Give the extent of all Plasmodium falciparum-infected red blood cells.
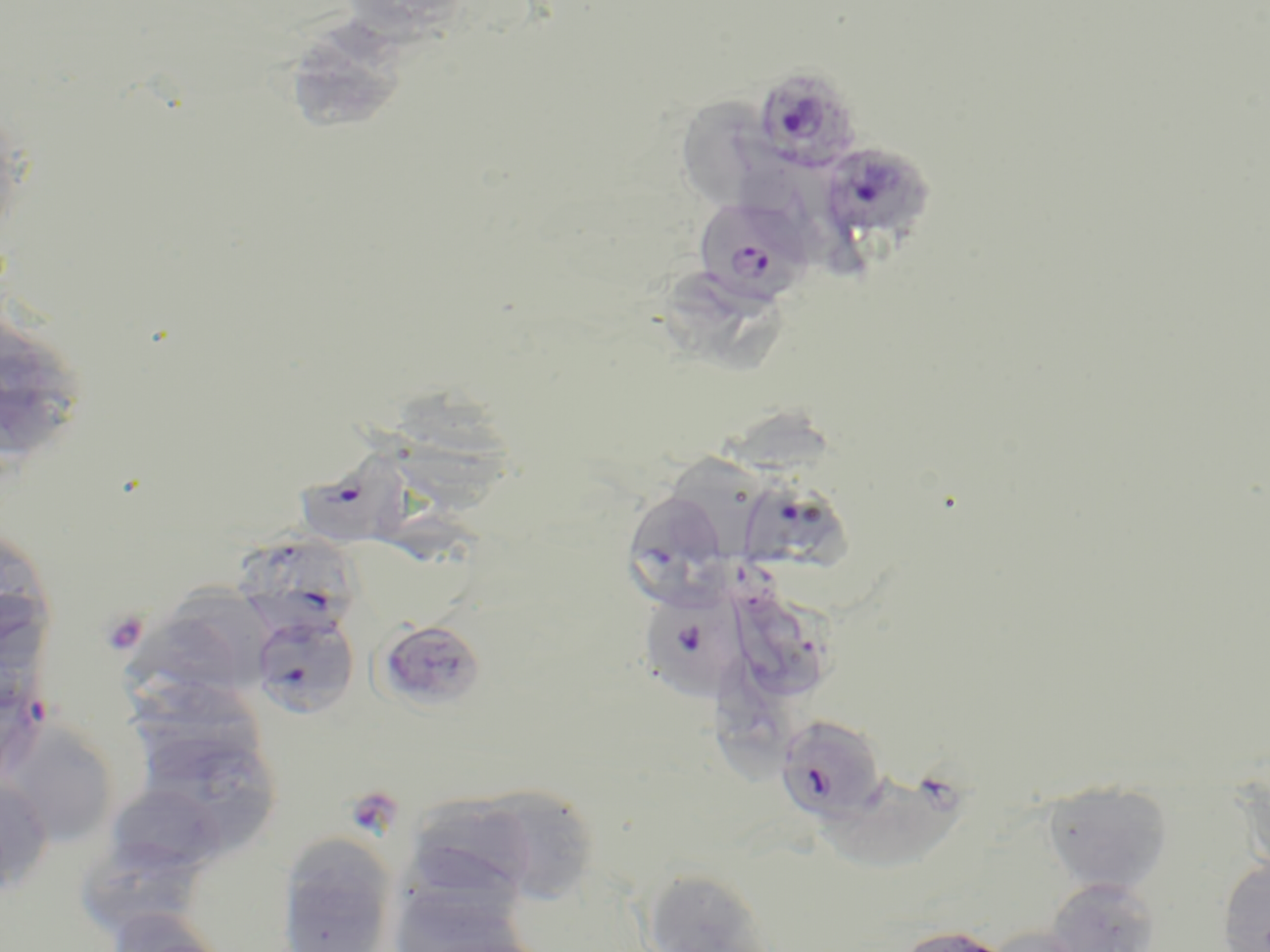
Approximate bounding boxes as (x1,y1)-(x2,y2) corner pairs in pixels.
Plasmodium falciparum-infected red blood cells: (752,65)-(864,173), (818,142)-(933,245), (693,197)-(811,305), (300,449)-(422,555), (744,474)-(853,618), (628,485)-(728,620), (239,535)-(356,644), (647,587)-(753,703), (250,609)-(360,719), (375,618)-(487,713), (0,670)-(53,783), (774,713)-(888,824), (828,771)-(975,868).

Uninfected red blood cell locations: (295,23)-(404,131), (681,94)-(787,208), (0,96)-(28,253), (745,158)-(854,270), (672,272)-(793,382), (1,320)-(81,460), (377,378)-(523,519), (720,398)-(847,491), (674,447)-(772,557), (0,524)-(56,655), (173,572)-(274,682), (739,592)-(828,691), (129,625)-(240,721), (717,655)-(801,792), (2,720)-(120,848), (145,735)-(276,849), (0,777)-(54,895), (1042,781)-(1173,895), (106,782)-(227,876), (397,790)-(568,911), (277,833)-(398,952), (75,836)-(206,940), (1217,858)-(1270,952), (641,867)-(776,952), (1045,877)-(1161,952), (387,883)-(537,952), (105,908)-(229,952), (892,924)-(1017,952), (983,927)-(1094,952). Platelet locations: (100,609)-(149,656), (354,791)-(396,834). Slide-level diagnosis: Plasmodium falciparum. Single field of view. Image is 1270×952 pixels. 1000x magnification. Thin blood film. May-Grünwald-Giemsa stain. Light microscopy.